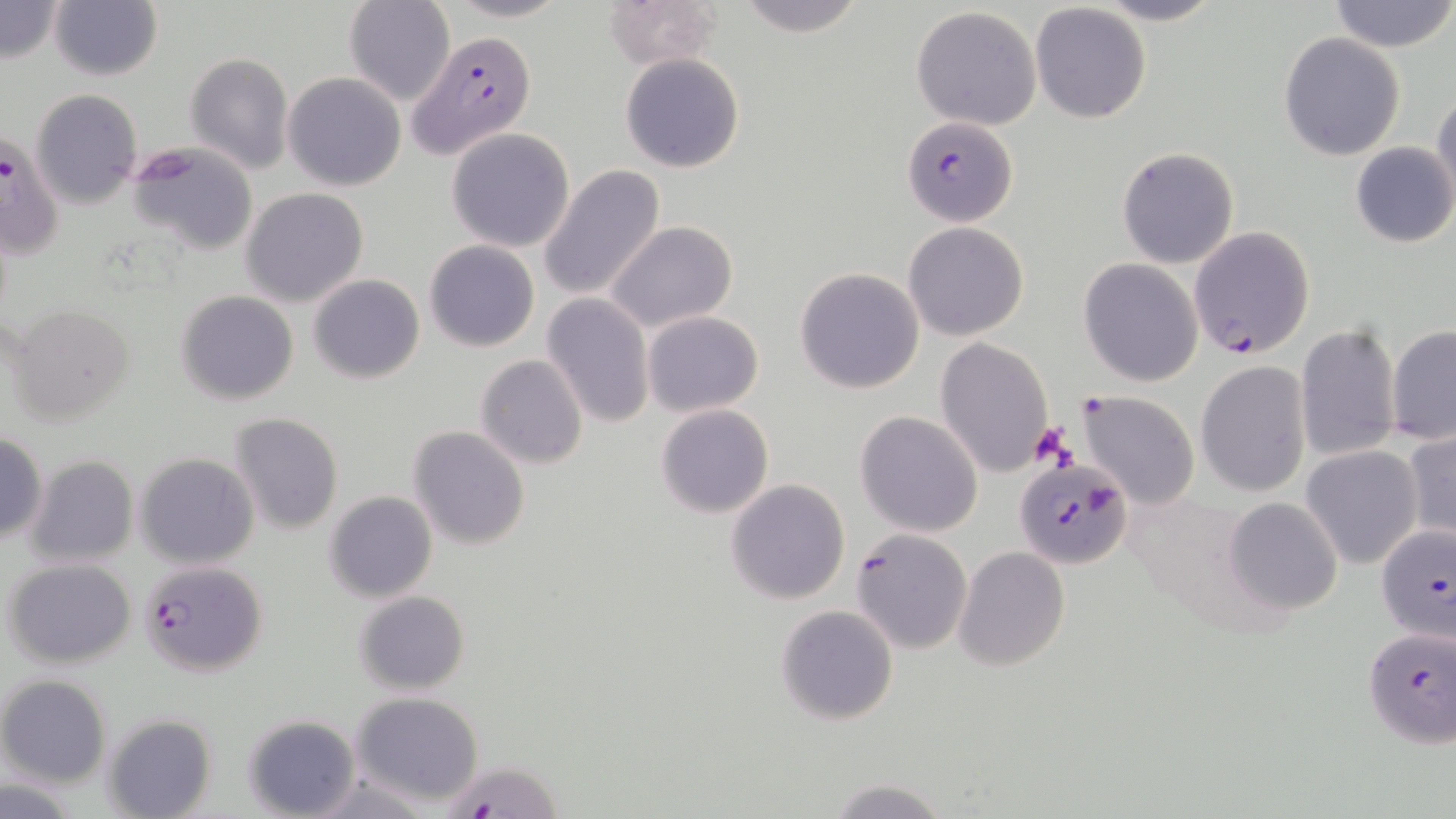

Summary:
  - Coordinate format: approximate bounding boxes as (x1, y1, x2, y2) in pixels
  - Plasmodium falciparum-infected red blood cell locations: (407, 30, 538, 158), (903, 115, 1017, 226), (0, 131, 64, 263), (1189, 225, 1314, 359), (1015, 457, 1132, 568), (1375, 525, 1456, 645), (851, 527, 973, 654), (138, 560, 269, 677), (1360, 624, 1456, 750), (438, 758, 563, 817)
  - Uninfected red blood cell locations: (49, 0, 163, 82), (344, 0, 454, 107), (438, 0, 574, 23), (733, 0, 867, 38), (1088, 0, 1227, 26), (1330, 0, 1455, 52), (0, 1, 65, 63), (603, 2, 725, 72), (1030, 3, 1152, 124), (911, 6, 1043, 130), (1279, 32, 1405, 159), (185, 53, 295, 174), (619, 54, 745, 173), (282, 72, 407, 192), (31, 89, 142, 208), (1432, 89, 1456, 205), (446, 127, 575, 252), (125, 140, 259, 256), (1350, 142, 1456, 248), (1117, 147, 1240, 267), (539, 164, 666, 301), (241, 188, 369, 308), (605, 220, 737, 334), (903, 221, 1029, 341), (424, 240, 539, 352), (1078, 258, 1203, 387), (794, 267, 925, 393), (309, 275, 424, 384), (176, 291, 300, 406), (540, 293, 655, 430), (5, 303, 137, 425), (643, 310, 763, 416), (1295, 321, 1403, 465), (1386, 324, 1456, 446), (936, 336, 1053, 477), (474, 354, 590, 469), (1196, 361, 1311, 497), (1076, 389, 1201, 509), (655, 404, 774, 518), (855, 410, 983, 537), (228, 412, 344, 534), (407, 425, 530, 551), (1402, 430, 1456, 545), (0, 432, 48, 544), (1300, 445, 1423, 569), (24, 454, 140, 568), (134, 454, 259, 569), (725, 479, 851, 604), (324, 491, 437, 603), (1224, 496, 1344, 615), (954, 546, 1071, 670), (4, 558, 138, 669), (353, 590, 471, 695), (775, 604, 900, 726), (0, 675, 112, 788), (350, 692, 484, 808), (242, 711, 361, 818), (102, 714, 216, 819), (0, 777, 84, 816), (825, 778, 951, 817)
  - Platelet locations: (1028, 422, 1074, 468)
  - Slide-level diagnosis: Plasmodium falciparum
  - Image size: 1456×819 pixels
  - Stain: May-Grünwald-Giemsa
  - Magnification: 1000x
  - Modality: optical microscopy
  - Field of view: one of a larger specimen
  - Preparation: thin blood smear